Point out each Plasmodium parasite.
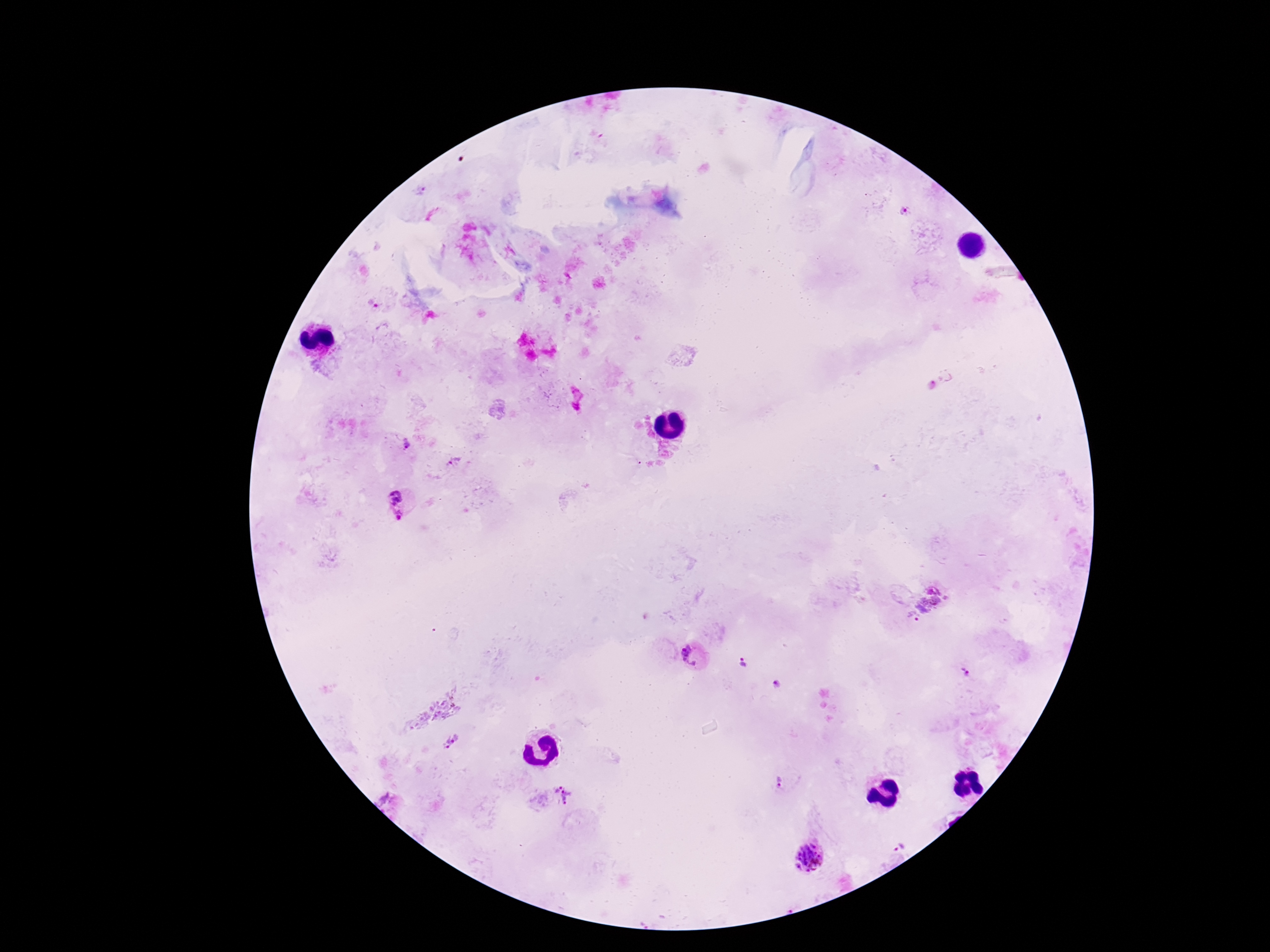
Approximate centers as (x, y) in pixels.
Plasmodium parasites: (420, 191), (904, 212), (372, 305), (405, 444), (454, 463), (395, 496), (398, 516), (931, 598), (913, 617), (692, 655), (741, 663), (965, 673), (779, 686), (452, 741), (780, 783), (564, 795), (385, 800), (901, 847), (810, 856).

One field from this slide. 100x magnification. Thick blood smear. Smartphone photograph taken through the microscope eyepiece. Patient malaria status: positive. Image is 1270×952 pixels. Giemsa-stained preparation.